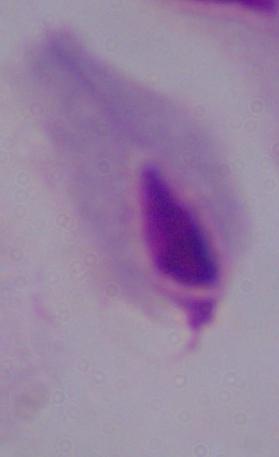
identification = trichomonad
magnification = 1000x
modality = micrograph